State the blood parasite species.
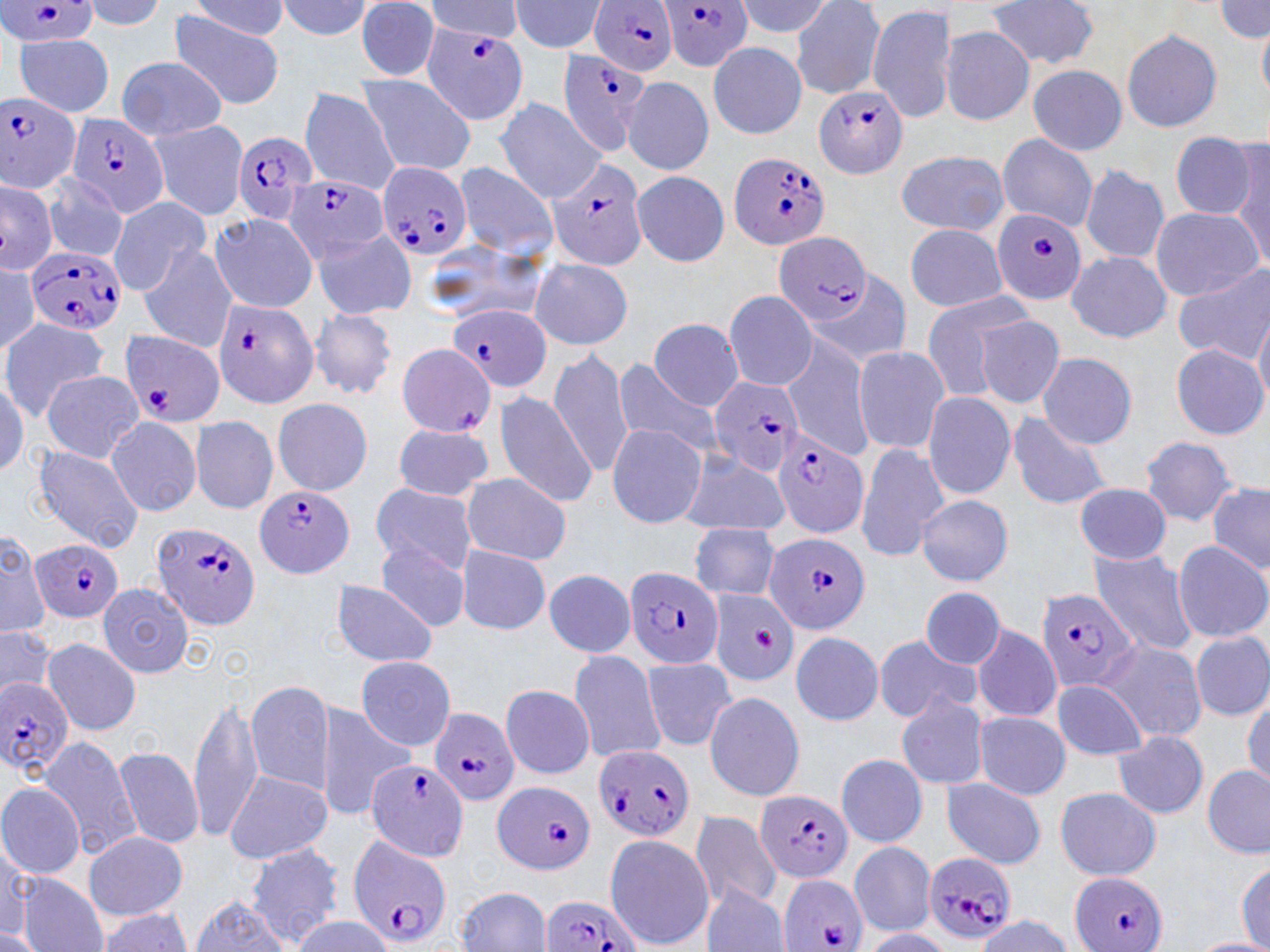
Plasmodium falciparum.

uninfected_red_blood_cell_locations: 'approximate bounding boxes as (x1,y1)-(x2,y2) corner pairs in pixels: (508,0)-(611,56), (732,0)-(833,38), (789,0)-(886,99), (75,1)-(167,32), (276,1)-(376,40), (354,1)-(441,80), (425,1)-(525,41), (187,2)-(291,42), (988,2)-(1101,71), (1215,2)-(1269,40), (867,4)-(956,122), (167,13)-(286,110), (1257,18)-(1269,108), (939,25)-(1035,126), (1122,29)-(1223,133), (14,34)-(115,116), (708,41)-(806,137), (115,58)-(229,140), (1028,64)-(1128,155), (356,74)-(477,175), (622,76)-(714,175), (298,87)-(399,194), (495,96)-(607,203), (148,118)-(251,220), (1168,131)-(1258,219), (996,133)-(1097,232), (1230,140)-(1269,266), (893,151)-(1010,235), (453,161)-(558,261), (1078,164)-(1170,264), (632,170)-(730,265), (38,175)-(130,263), (0,180)-(57,275), (107,196)-(212,297), (1151,206)-(1262,300), (206,212)-(320,314), (905,223)-(1007,312), (310,226)-(416,321), (417,238)-(545,329), (138,242)-(237,352), (1065,250)-(1172,343), (528,256)-(633,351), (0,258)-(41,356), (802,267)-(913,369), (1175,268)-(1270,363), (724,289)-(818,392), (918,291)-(1034,401), (1239,296)-(1270,395), (1253,306)-(1270,410), (308,309)-(398,399), (975,313)-(1066,409), (0,316)-(109,419), (650,319)-(744,411), (780,333)-(876,461), (1172,344)-(1268,439), (852,346)-(952,455), (549,347)-(635,478), (1036,351)-(1137,449), (611,359)-(722,456), (0,368)-(28,476), (39,369)-(145,461), (493,389)-(598,505), (923,392)-(1016,499), (271,396)-(373,495), (1007,410)-(1112,511), (105,413)-(202,517), (190,415)-(279,515), (393,423)-(495,501), (605,424)-(707,528), (1138,436)-(1241,525), (30,442)-(144,553), (855,442)-(951,562), (677,450)-(790,537), (458,471)-(572,566), (370,481)-(476,575), (1073,482)-(1173,565), (1207,482)-(1270,575), (916,495)-(1014,586), (688,521)-(782,602), (0,529)-(47,639), (375,541)-(470,632), (1171,541)-(1270,643), (457,545)-(550,635), (1086,548)-(1198,655), (544,568)-(636,657), (330,579)-(437,669), (97,582)-(194,677), (919,585)-(1007,669), (969,622)-(1062,722), (0,627)-(56,703), (790,630)-(884,726), (1191,632)-(1270,721), (872,635)-(979,722), (42,637)-(140,735), (1095,639)-(1206,742), (568,649)-(669,765), (356,656)-(456,751), (641,656)-(737,751), (1051,678)-(1148,761), (246,680)-(336,792), (499,683)-(595,778), (1244,691)-(1270,790), (703,692)-(807,802), (895,692)-(989,789), (188,694)-(263,844), (315,700)-(416,820), (973,710)-(1069,799), (1113,730)-(1209,819), (38,738)-(139,857), (113,746)-(204,848), (836,754)-(928,847), (1201,765)-(1269,858), (224,770)-(333,865), (939,779)-(1047,870), (0,782)-(86,880), (1055,787)-(1162,880), (688,811)-(784,908), (84,831)-(188,921), (604,833)-(713,947), (0,838)-(31,939), (850,841)-(935,935), (246,843)-(346,945), (1234,861)-(1269,948), (16,874)-(107,952), (702,886)-(790,952), (456,887)-(552,951), (188,896)-(291,951), (91,908)-(195,950), (290,914)-(391,951), (969,915)-(1078,952), (0,926)-(47,951), (857,928)-(953,951), (1190,937)-(1270,952)'
preparation: thin blood smear
modality: light microscopy
image_size: 1270×952 pixels
field_of_view: one of a larger specimen
plasmodium_falciparum_infected_red_blood_cell_locations: 'approximate bounding boxes as (x1,y1)-(x2,y2) corner pairs in pixels: (0,0)-(101,47), (661,1)-(753,72), (589,3)-(677,76), (419,23)-(529,125), (558,51)-(651,154), (815,86)-(909,179), (0,91)-(83,193), (68,114)-(171,219), (228,130)-(317,228), (730,149)-(832,250), (544,155)-(649,271), (376,161)-(472,262), (284,173)-(390,261), (993,210)-(1087,305), (771,231)-(871,326), (25,245)-(126,337), (212,299)-(319,407), (447,304)-(552,393), (120,330)-(224,427), (708,375)-(801,477), (772,431)-(869,538), (256,484)-(356,579), (152,522)-(260,629), (763,532)-(872,635), (30,537)-(125,623), (626,565)-(724,669), (1036,587)-(1140,694), (0,677)-(75,775), (430,708)-(519,806), (594,746)-(692,841), (366,759)-(469,863), (494,782)-(596,875), (755,789)-(852,884), (348,834)-(451,947), (921,852)-(1018,943), (1073,872)-(1166,952), (778,874)-(868,952), (540,893)-(641,952)'
magnification: 1000x
stain: May-Grünwald-Giemsa